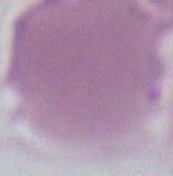

Summary:
  - Modality: micrograph
  - Magnification: 1000x
  - Identification: erythrocyte